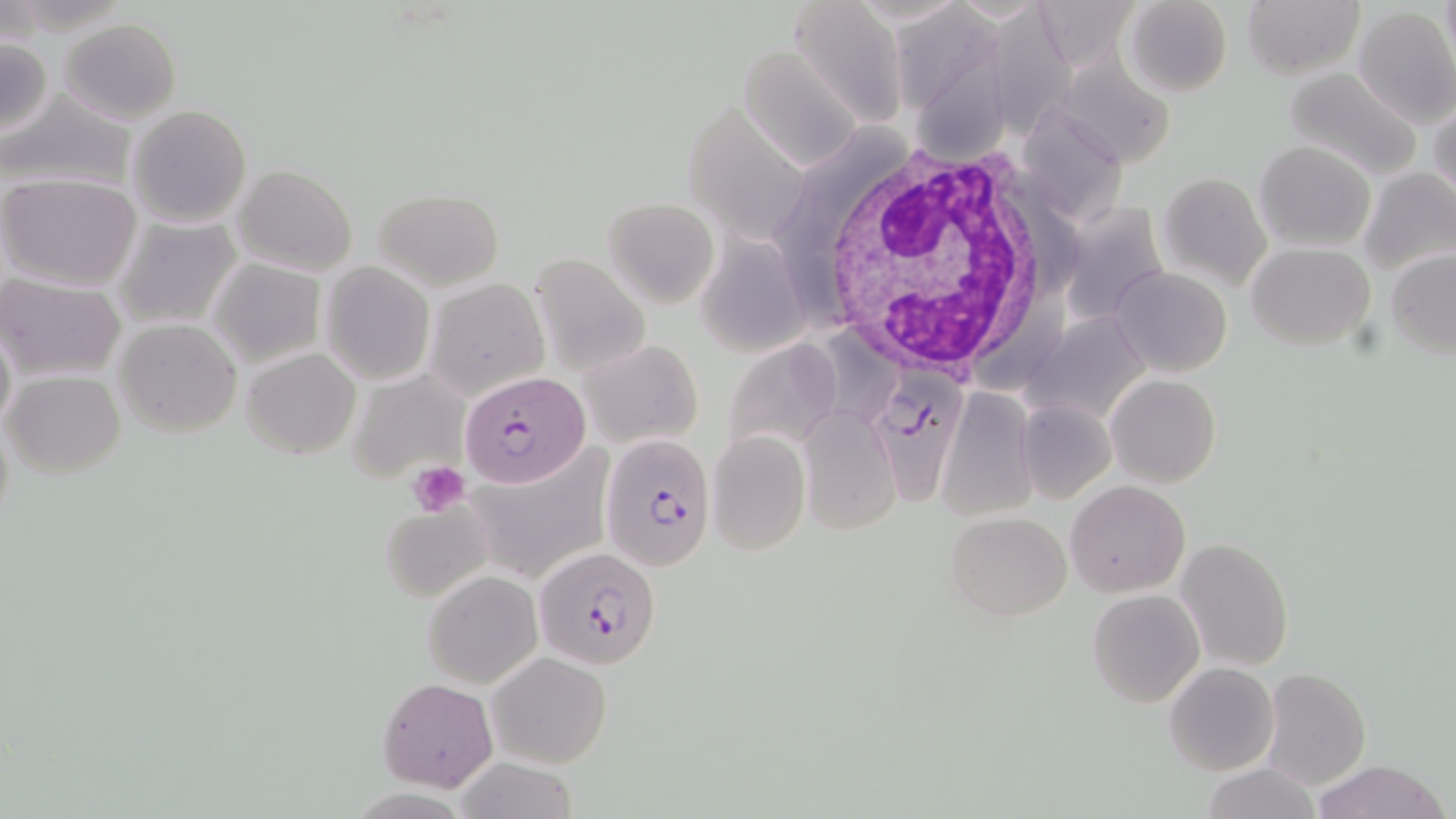
slide_level_diagnosis: Plasmodium falciparum
stain: May-Grünwald-Giemsa
image_size: 1456×819 pixels
magnification: 1000x
plasmodium_falciparum_infected_red_blood_cell_locations: 'approximate bounding boxes as (x1, y1, x2, y2) in pixels: (866, 363, 987, 515), (459, 370, 590, 485), (600, 436, 717, 571), (532, 545, 661, 671)'
modality: light microscopy
white_blood_cell_locations: 'approximate bounding boxes as (x1, y1, x2, y2) in pixels: (799, 134, 1055, 373)'
uninfected_red_blood_cell_locations: 'approximate bounding boxes as (x1, y1, x2, y2) in pixels: (788, 0, 908, 129), (1124, 0, 1232, 97), (1241, 0, 1363, 79), (1353, 6, 1456, 127), (983, 7, 1085, 149), (887, 8, 1001, 106), (61, 17, 181, 124), (0, 37, 53, 140), (737, 45, 870, 172), (918, 47, 1014, 165), (1059, 55, 1172, 168), (1280, 65, 1425, 181), (0, 86, 136, 198), (1429, 98, 1456, 209), (128, 104, 252, 229), (674, 109, 815, 252), (1027, 118, 1136, 233), (1254, 140, 1377, 251), (233, 165, 358, 277), (1360, 167, 1456, 280), (0, 172, 142, 290), (1158, 173, 1271, 293), (373, 188, 505, 291), (604, 197, 721, 306), (1074, 209, 1172, 324), (114, 215, 241, 329), (709, 239, 810, 344), (1247, 242, 1375, 350), (1386, 249, 1456, 359), (528, 251, 650, 379), (208, 256, 325, 368), (321, 262, 434, 384), (1110, 266, 1233, 378), (0, 274, 125, 382), (426, 278, 549, 399), (1025, 316, 1145, 425), (114, 317, 242, 438), (1, 319, 16, 442), (580, 338, 705, 448), (733, 344, 842, 460), (242, 346, 360, 458), (348, 369, 470, 486), (4, 370, 125, 478), (1105, 374, 1221, 488), (936, 389, 1037, 521), (1018, 399, 1115, 503), (798, 407, 900, 536), (707, 430, 811, 555), (484, 445, 611, 576), (1066, 481, 1190, 597), (382, 504, 491, 602), (944, 510, 1072, 620), (1175, 537, 1295, 670), (423, 570, 542, 689), (1088, 589, 1205, 708), (487, 651, 612, 768), (1164, 662, 1279, 776), (1261, 666, 1370, 789), (379, 679, 497, 791), (450, 758, 583, 818), (1311, 759, 1450, 819), (1197, 764, 1322, 818)'
field_of_view: single
preparation: thin blood film
platelet_locations: 'approximate bounding boxes as (x1, y1, x2, y2) in pixels: (409, 460, 471, 514)'